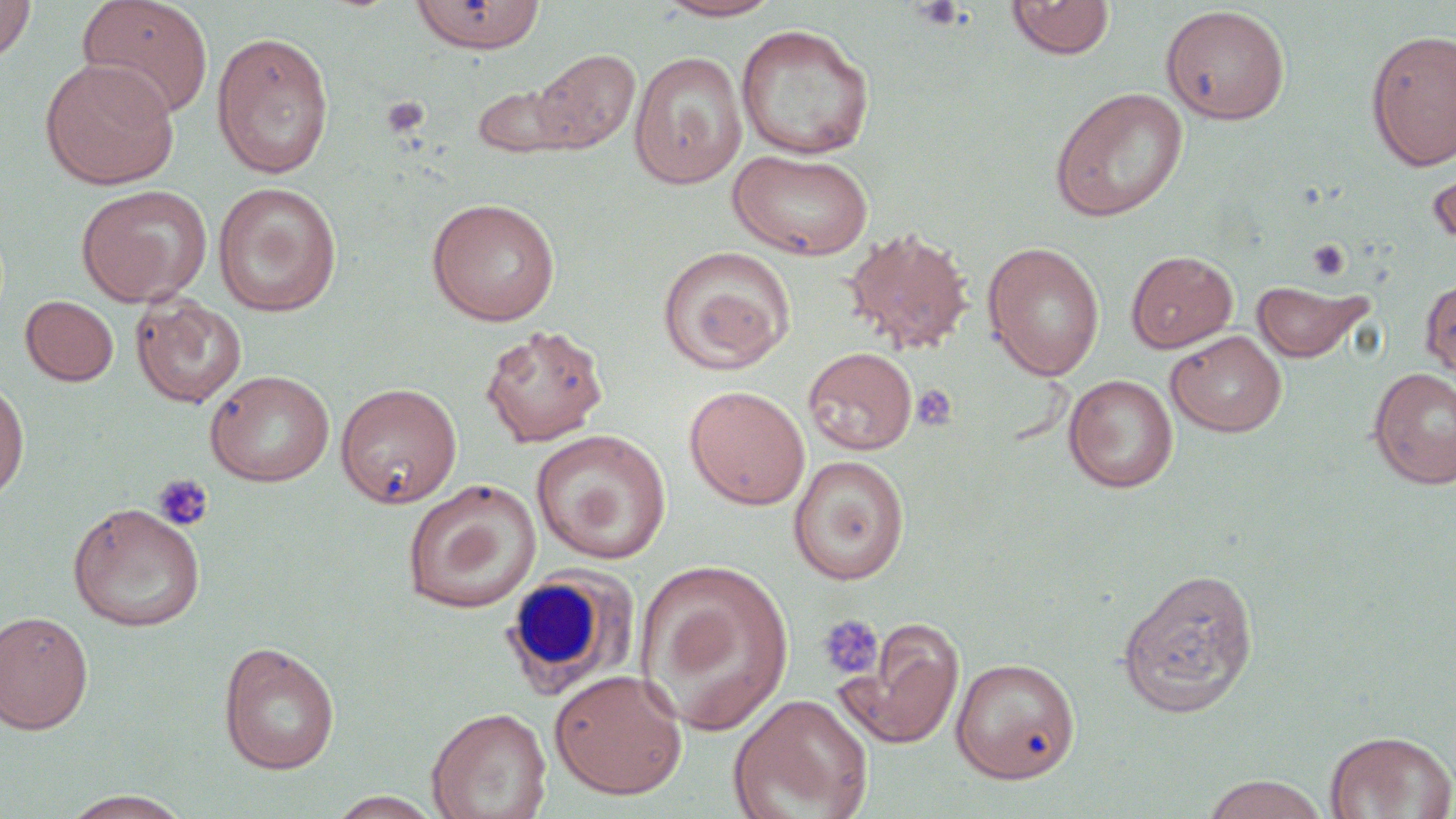

Summary:
  - Coordinate format: approximate bounding boxes as (x1,y1)-(x2,y2) corner pairs in pixels
  - Platelet locations: (909,0)-(966,30), (381,95)-(430,138), (1306,239)-(1351,280), (912,385)-(956,430), (151,473)-(214,532), (817,614)-(884,681)
  - White blood cell locations: (499,566)-(636,701)
  - Uninfected red blood cell locations: (0,0)-(37,62), (76,0)-(213,121), (411,0)-(546,54), (655,0)-(784,21), (1005,0)-(1115,60), (1160,5)-(1291,125), (735,23)-(876,161), (1364,28)-(1456,171), (211,30)-(335,179), (532,47)-(641,154), (628,51)-(747,189), (39,57)-(179,190), (473,84)-(576,158), (1049,86)-(1189,222), (728,148)-(874,261), (1426,152)-(1456,258), (212,182)-(343,318), (75,185)-(213,307), (426,198)-(561,326), (842,226)-(975,356), (982,242)-(1105,381), (657,245)-(796,375), (1125,250)-(1238,353), (1420,276)-(1456,386), (1250,278)-(1373,364), (129,293)-(248,408), (20,295)-(119,386), (480,323)-(609,448), (1165,330)-(1287,437), (804,347)-(917,456), (1368,366)-(1456,489), (204,369)-(334,487), (0,373)-(29,506), (1064,374)-(1178,492), (335,382)-(462,508), (684,385)-(810,510), (530,429)-(671,564), (788,454)-(910,584), (402,479)-(541,614), (67,501)-(206,632), (634,558)-(794,734), (1116,567)-(1259,718), (0,610)-(94,734), (839,618)-(965,749), (218,640)-(340,775), (951,658)-(1080,783), (549,669)-(687,800), (728,694)-(873,819), (426,706)-(552,819), (1324,729)-(1456,818), (1201,774)-(1329,818), (59,790)-(194,818), (326,791)-(444,818)
  - Slide-level diagnosis: negative for blood parasites
  - Stain: May-Grünwald-Giemsa
  - Field of view: one of a larger specimen
  - Magnification: 1000x
  - Image size: 1456×819 pixels
  - Preparation: thin blood film
  - Modality: light microscopy